Comment on the morphology of the erythrocytes.
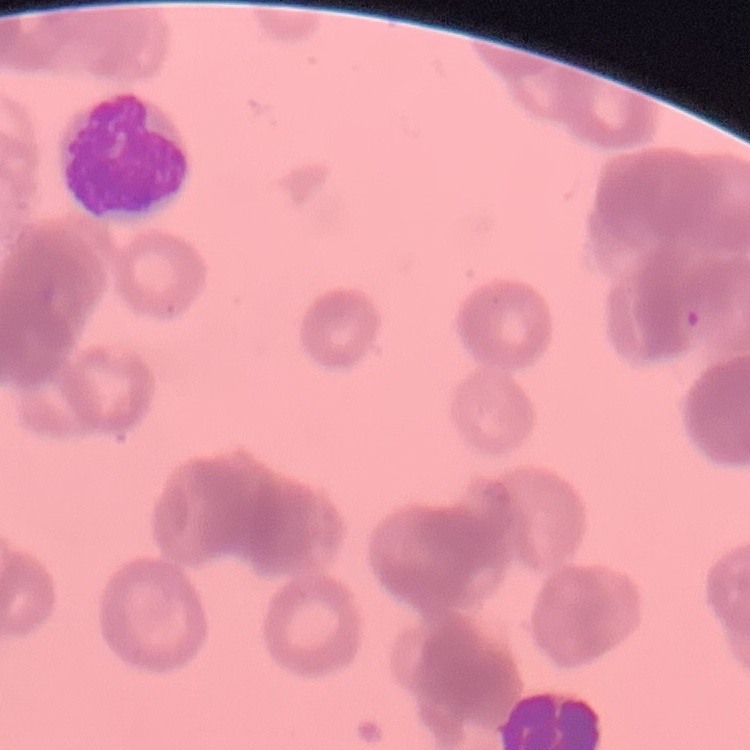
They show rouleaux formation.

One tile cut from a larger photomicrograph. Thin blood smear. Field's or Giemsa stain.